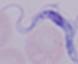
Captured at 1000x magnification. Micrograph. A trypanosome is shown.